Identify the blood parasite species.
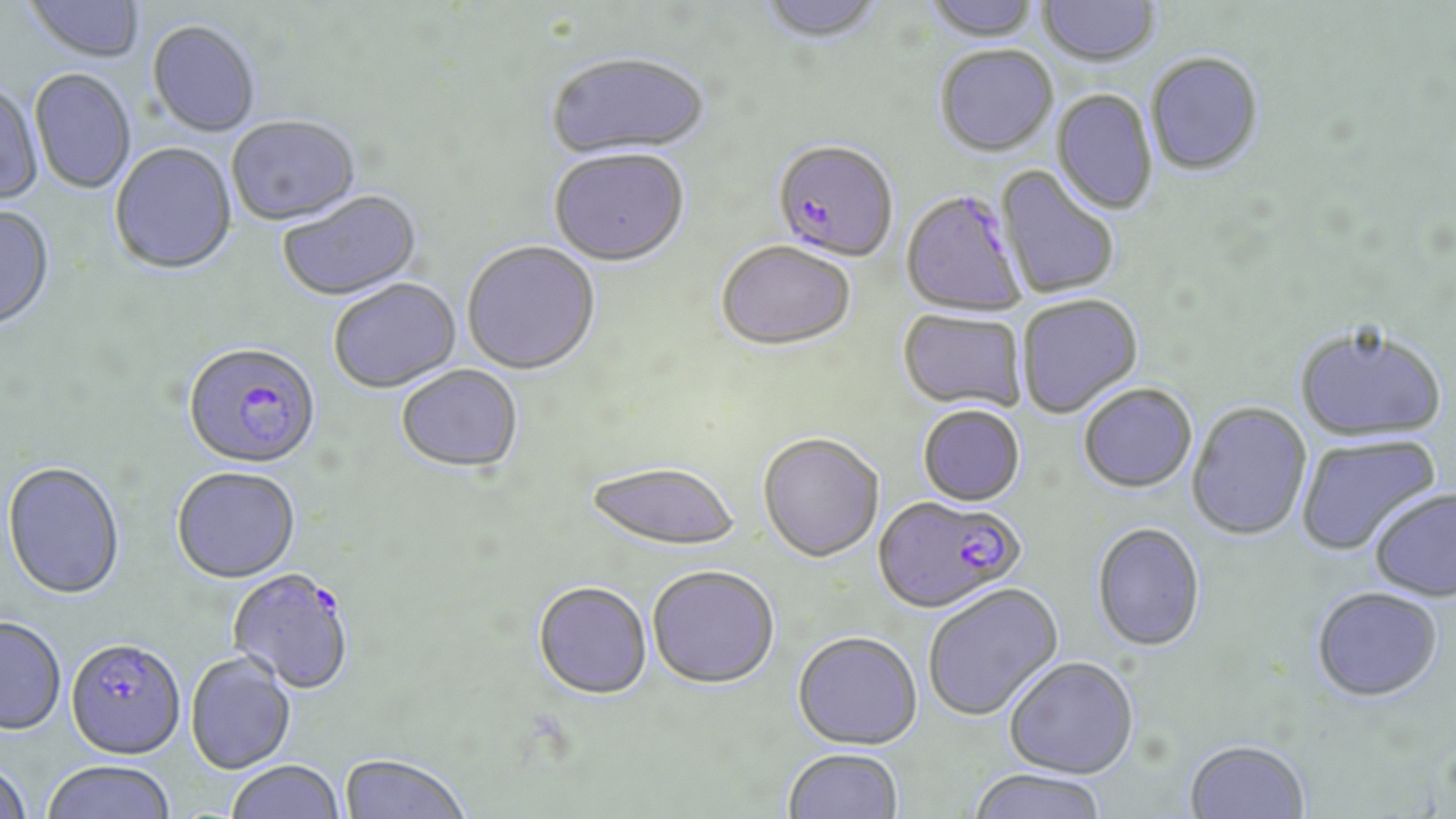
Plasmodium falciparum.

uninfected_red_blood_cell_locations: 'approximate bounding boxes as [x1, y1, x2, y2] in pixels: [25, 0, 145, 63], [757, 0, 884, 46], [924, 0, 1041, 43], [1038, 0, 1161, 67], [147, 21, 261, 138], [935, 46, 1058, 157], [1146, 52, 1264, 175], [544, 53, 711, 161], [30, 69, 136, 194], [0, 83, 44, 205], [1051, 89, 1157, 215], [226, 116, 361, 227], [110, 143, 237, 276], [548, 151, 690, 269], [1000, 163, 1126, 298], [278, 191, 423, 303], [0, 206, 56, 331], [715, 242, 856, 352], [462, 243, 601, 376], [329, 280, 462, 394], [1017, 294, 1143, 418], [898, 309, 1028, 412], [1295, 322, 1447, 442], [396, 366, 523, 475], [1078, 382, 1197, 492], [1187, 401, 1312, 541], [918, 405, 1026, 506], [757, 433, 884, 562], [1296, 434, 1441, 555], [585, 461, 741, 552], [2, 462, 125, 601], [171, 467, 301, 583], [1369, 487, 1456, 601], [1092, 522, 1207, 651], [647, 565, 780, 688], [532, 581, 652, 700], [922, 583, 1063, 722], [1311, 586, 1443, 701], [0, 615, 67, 735], [792, 631, 922, 748], [186, 652, 297, 774], [1004, 655, 1139, 778], [1184, 738, 1310, 819], [783, 747, 904, 819], [338, 753, 472, 818], [41, 760, 176, 819], [226, 760, 345, 819], [0, 762, 33, 819], [965, 768, 1109, 819]'
field_of_view: one of a larger specimen
image_size: 1456×819 pixels
plasmodium_falciparum_infected_red_blood_cell_locations: 'approximate bounding boxes as [x1, y1, x2, y2] in pixels: [772, 139, 899, 262], [901, 189, 1028, 317], [183, 341, 321, 470], [874, 494, 1025, 613], [227, 568, 356, 695], [65, 637, 185, 759]'
stain: May-Grünwald-Giemsa
modality: optical microscopy
preparation: thin blood smear
magnification: 1000x